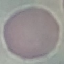

Summary:
  - Result: negative for malaria parasites
  - Stain: Giemsa
  - Preparation: thin smear
  - Image type: automatically extracted cell patch, resized to 64 × 64 pixels
  - Capture: smartphone camera at the microscope eyepiece